State the preparation type.
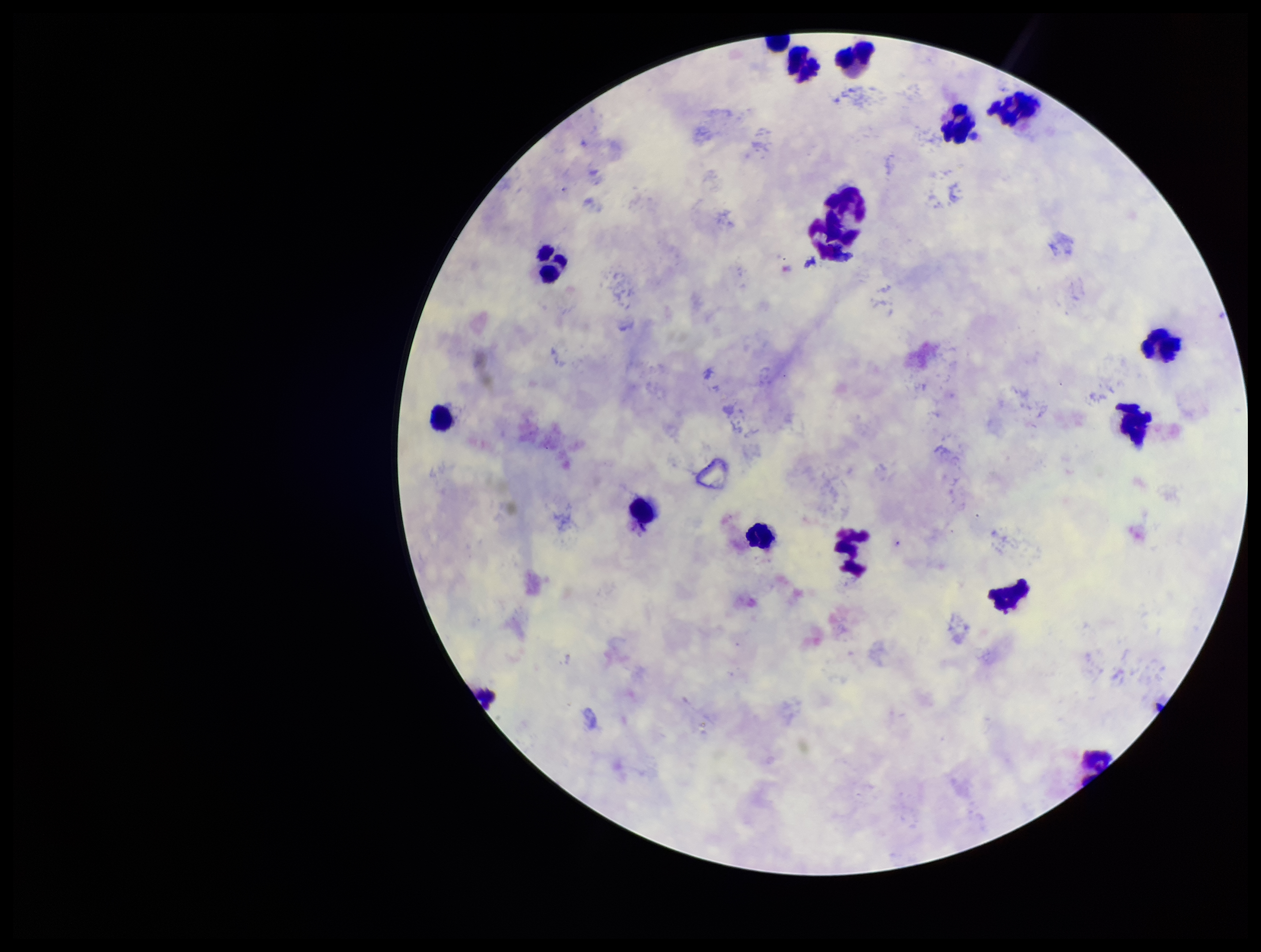

Thick.

{
  "field_of_view": "single",
  "image_size": "1261×952 pixels",
  "stain": "Giemsa",
  "leukocyte_count": 17,
  "plasmodium_parasites": "none identified",
  "capture": "smartphone photograph through the microscope eyepiece",
  "parasite_count": 0,
  "patient_malaria_status": "positive",
  "species_reported_for_this_patient": "Plasmodium vivax"
}